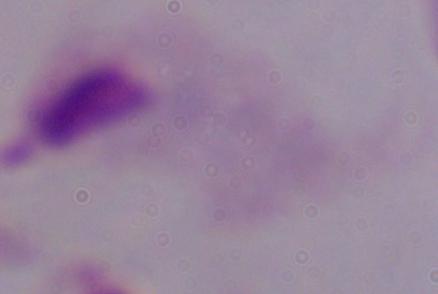
A trichomonad is shown. 1000x magnification. Micrograph.